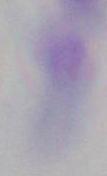
magnification: 1000x
modality: photomicrograph
identification: Toxoplasma gondii